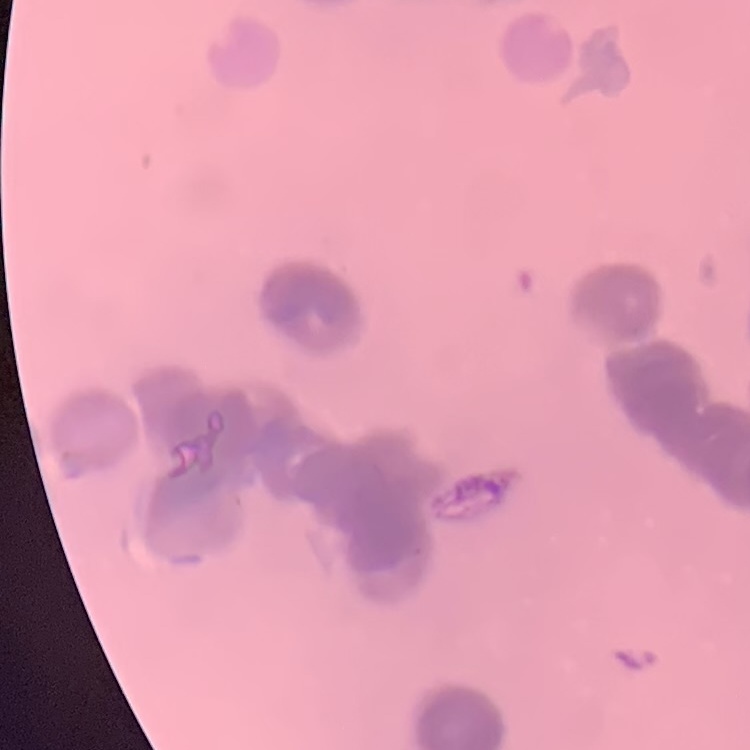
Summary:
  - Erythrocyte morphology: rouleaux formation
  - Image type: one tile cut from a larger photomicrograph
  - Stain: Field's or Giemsa
  - Preparation: thin blood film